Give the position of every Plasmodium parasite.
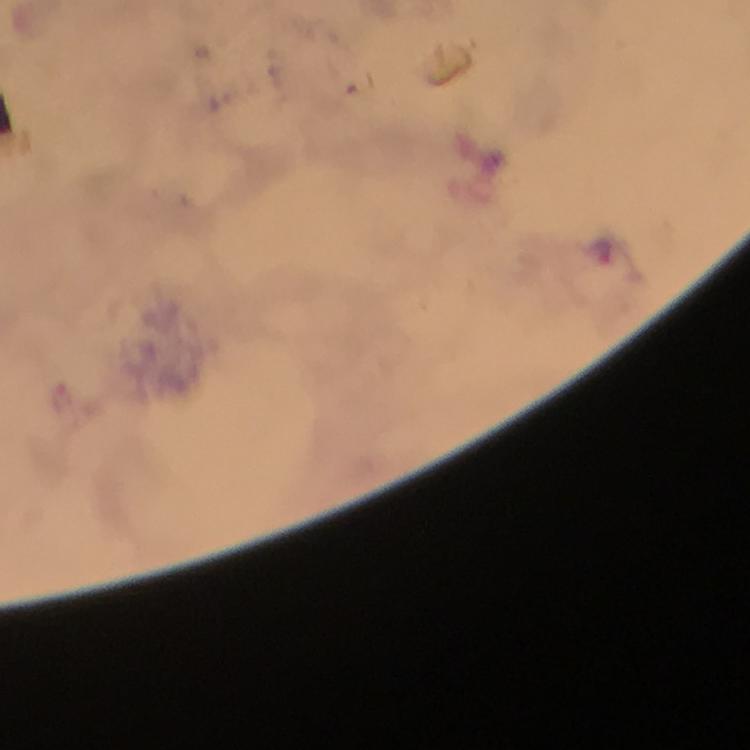
Approximate object centers, in pixels from the top-left corner.
Plasmodium parasites: (x=600, y=249), (x=60, y=398).

stain: Giemsa
preparation: thick blood film
capture: smartphone camera through the microscope
immersion_oil: used
cropped_from: one field of view
context: from a malaria diagnostic workup
image_size: 750×750 pixels
magnification: 100x